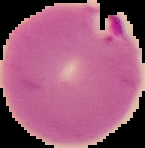

image size = 145×148 pixels
preparation = thin blood smear
image type = segmented cell region on a black background
malaria status = parasitized